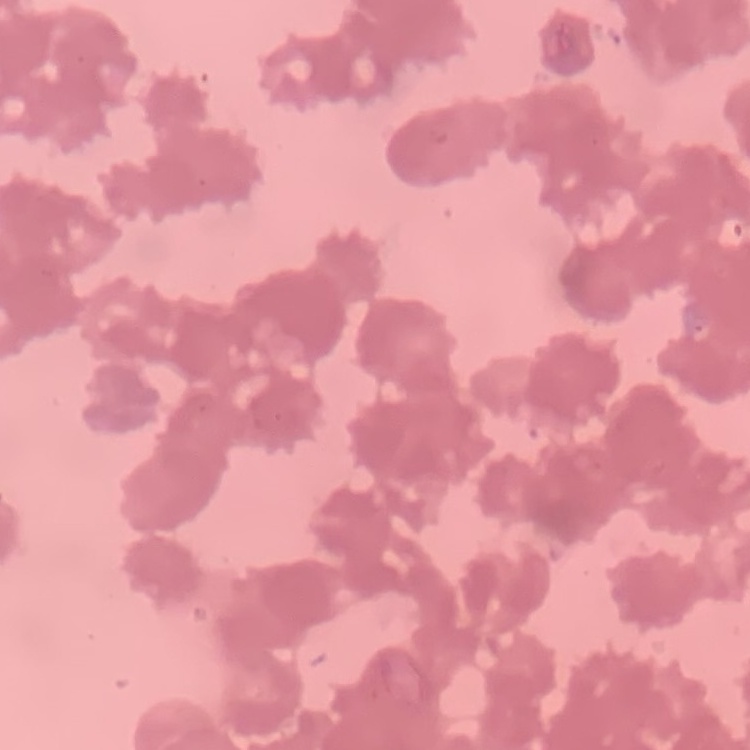 The red blood cells show rouleaux formation. Thin blood smear. Field's or Giemsa stain. Square crop of a larger photomicrograph.